Name the parasite shown.
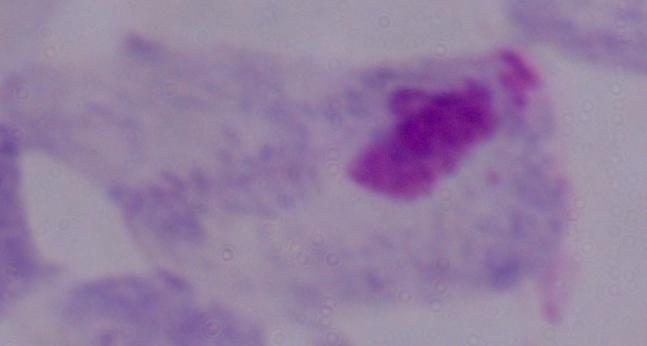
This is a trichomonad.

1000x magnification. Photomicrograph.